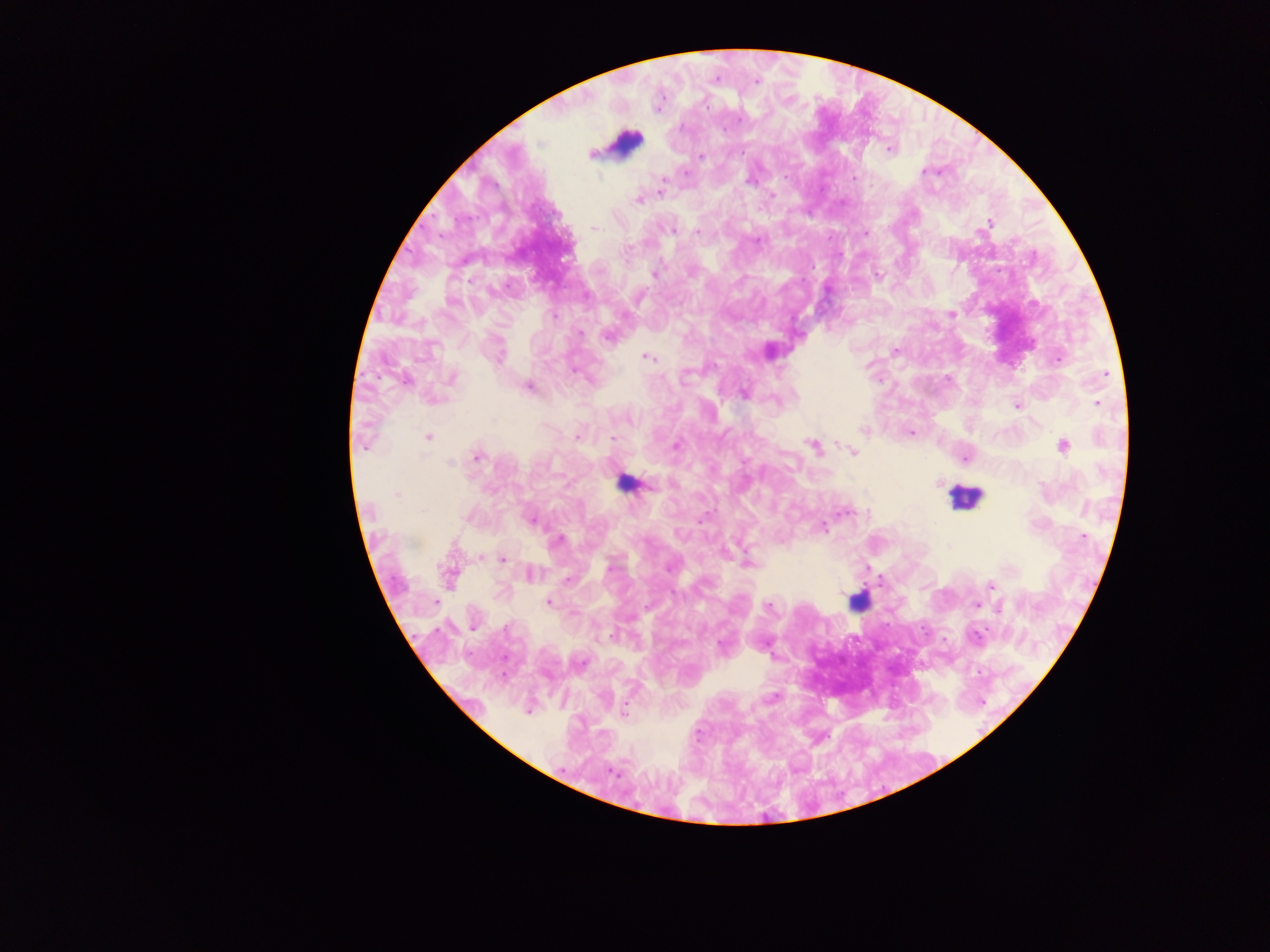 Approximate centers as (x, y) in pixels. Plasmodium parasite locations: (716, 78), (757, 81), (888, 149), (591, 155), (701, 156), (925, 172), (686, 174), (785, 176), (749, 180), (662, 183), (660, 191), (638, 200), (988, 223), (594, 227), (672, 230), (697, 231), (866, 232), (758, 240), (628, 250), (654, 274), (878, 275), (951, 314), (555, 317), (581, 332), (607, 337), (894, 350), (770, 351), (499, 358), (647, 358), (1057, 360), (574, 371), (1106, 374), (685, 377), (451, 378), (405, 380), (529, 386), (743, 394), (1097, 403), (1017, 405), (629, 420), (863, 430), (911, 433), (429, 437), (577, 437), (612, 437), (363, 444), (676, 445), (1063, 446), (813, 447), (852, 452), (477, 458), (965, 458), (450, 462), (939, 483), (651, 487), (397, 495), (846, 512), (530, 520), (823, 527), (1085, 537), (558, 539), (948, 545), (481, 556), (504, 559), (748, 563), (609, 569), (530, 574), (449, 575), (568, 579), (990, 586), (549, 602), (977, 605), (769, 607), (999, 609), (611, 635), (976, 636), (722, 644), (979, 673), (774, 697), (527, 711), (625, 712), (612, 771). Leukocyte locations: (625, 143), (626, 485), (965, 497), (857, 608). Image is 1270×952 pixels. Collected in Ghana. One field of view. Mobile-phone photograph taken through the microscope. Thick blood smear.